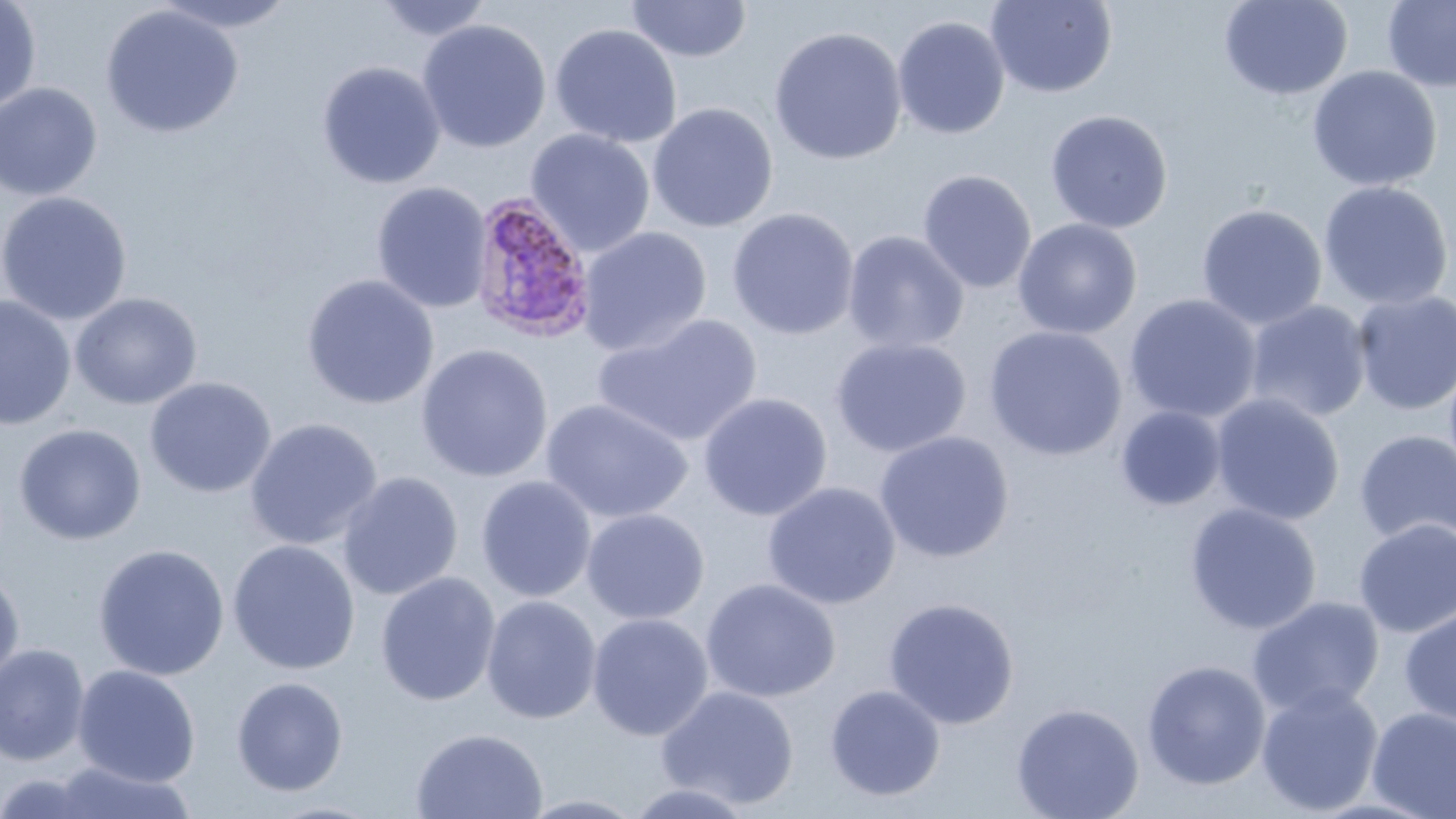
slide-level diagnosis = Plasmodium ovale
uninfected red blood cell locations = approximate bounding boxes as [x1, y1, x2, y2] in pixels: [150, 0, 300, 34], [372, 0, 496, 41], [1218, 0, 1353, 100], [0, 1, 42, 115], [625, 1, 752, 63], [985, 1, 1118, 98], [1381, 1, 1456, 92], [100, 5, 244, 138], [892, 15, 1011, 140], [417, 19, 552, 153], [549, 23, 683, 148], [768, 26, 907, 165], [317, 61, 446, 189], [1307, 65, 1442, 192], [0, 82, 103, 201], [647, 102, 778, 233], [1044, 109, 1174, 234], [525, 128, 656, 256], [917, 169, 1037, 293], [1317, 180, 1454, 311], [371, 182, 492, 313], [0, 191, 132, 325], [1196, 204, 1327, 330], [727, 207, 860, 340], [1012, 218, 1142, 339], [577, 226, 712, 357], [842, 230, 970, 354], [301, 274, 439, 409], [1351, 290, 1456, 416], [70, 292, 203, 410], [1124, 293, 1262, 424], [0, 295, 76, 430], [1244, 300, 1373, 423], [593, 313, 763, 448], [983, 326, 1128, 461], [830, 336, 972, 457], [416, 343, 554, 483], [144, 376, 277, 498], [698, 392, 833, 521], [1210, 393, 1345, 526], [541, 398, 693, 523], [1115, 406, 1226, 511], [244, 417, 383, 550], [14, 423, 147, 545], [1354, 430, 1456, 548], [874, 431, 1014, 563], [337, 471, 464, 601], [476, 475, 597, 602], [762, 481, 902, 609], [1185, 502, 1322, 635], [581, 508, 710, 625], [1353, 518, 1456, 637], [227, 539, 361, 675], [93, 544, 230, 681], [0, 567, 25, 689], [375, 571, 502, 706], [701, 578, 840, 703], [481, 595, 602, 725], [883, 596, 1019, 729], [1246, 596, 1385, 718], [1399, 605, 1456, 729], [587, 613, 714, 741], [0, 643, 90, 766], [1141, 660, 1271, 790], [72, 664, 201, 787], [231, 676, 349, 796], [1255, 683, 1384, 816], [824, 684, 946, 801], [656, 685, 800, 809], [1010, 703, 1144, 819], [1367, 707, 1456, 819], [411, 728, 548, 819], [40, 762, 199, 819], [623, 782, 757, 819], [515, 793, 649, 818]
magnification = 1000x
field of view = single
preparation = thin blood film
stain = May-Grünwald-Giemsa
image size = 1456×819 pixels
modality = optical microscopy
Plasmodium ovale-infected red blood cell locations = approximate bounding boxes as [x1, y1, x2, y2] in pixels: [468, 191, 598, 343]